Locate and identify every blood parasite.
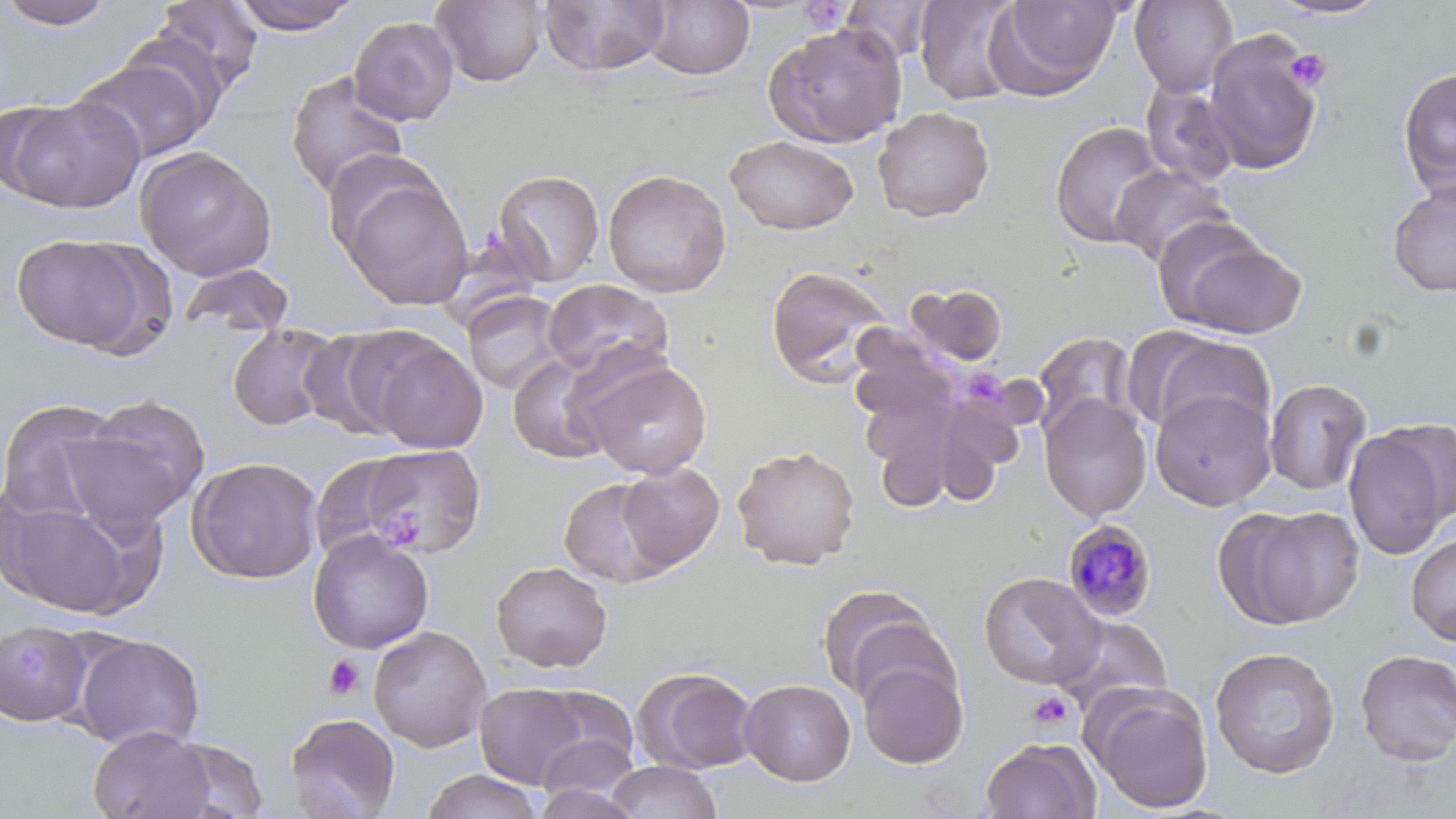

Approximate bounding boxes as (x1,y1)-(x2,y2) corner pairs in pixels.
Plasmodium malariae-infected red blood cells: (1062,519)-(1159,621).
No Plasmodium falciparum, Plasmodium ovale, Plasmodium vivax, Babesia divergens, or Trypanosoma brucei observed.

{
  "slide_level_diagnosis": "Plasmodium malariae",
  "image_size": "1456×819 pixels",
  "platelet_locations": "approximate bounding boxes as (x1,y1)-(x2,y2) corner pairs in pixels: (798,3)-(852,32), (1285,48)-(1332,93), (969,373)-(1004,406), (383,511)-(425,545), (16,644)-(54,678), (323,655)-(365,701), (1026,690)-(1075,732)",
  "stain": "May-Grünwald-Giemsa",
  "preparation": "thin blood smear",
  "modality": "light microscopy",
  "magnification": "1000x",
  "field_of_view": "one of a larger specimen",
  "uninfected_red_blood_cell_locations": "approximate bounding boxes as (x1,y1)-(x2,y2) corner pairs in pixels: (151,0)-(265,95), (228,0)-(363,35), (431,0)-(548,88), (537,0)-(671,78), (913,0)-(1024,105), (988,0)-(1123,99), (1129,0)-(1238,98), (2,1)-(116,29), (644,1)-(754,80), (839,1)-(939,62), (1264,1)-(1395,21), (348,16)-(459,125), (763,22)-(907,148), (1203,30)-(1325,176), (75,55)-(214,164), (1397,67)-(1456,197), (285,71)-(410,201), (1140,82)-(1241,187), (2,95)-(144,213), (872,107)-(995,222), (1049,121)-(1167,249), (725,135)-(859,235), (135,146)-(277,281), (1110,164)-(1233,267), (603,169)-(731,298), (492,170)-(605,287), (340,174)-(473,309), (1387,179)-(1456,296), (1163,230)-(1307,338), (11,232)-(163,357), (176,262)-(297,340), (765,264)-(894,388), (542,278)-(672,380), (906,283)-(1008,366), (462,291)-(567,395), (227,323)-(344,431), (298,326)-(414,441), (1134,330)-(1275,439), (1031,331)-(1140,443), (365,335)-(488,454), (507,352)-(615,465), (579,356)-(712,479), (1264,378)-(1371,495), (1150,389)-(1277,511), (70,394)-(211,529), (1039,395)-(1152,522), (0,399)-(124,523), (1343,424)-(1451,561), (359,443)-(485,558), (732,443)-(861,570), (309,453)-(422,562), (187,456)-(322,584), (617,462)-(725,572), (560,478)-(672,588), (2,494)-(149,618), (1222,504)-(1366,630), (307,530)-(434,654), (1406,533)-(1456,646), (490,561)-(613,673), (978,572)-(1104,690), (816,583)-(946,706), (1051,614)-(1174,717), (369,626)-(491,752), (0,627)-(107,726), (72,632)-(207,752), (1209,646)-(1341,779), (1354,649)-(1456,766), (855,654)-(969,769), (634,667)-(760,775), (739,679)-(856,786), (474,683)-(591,789), (529,684)-(639,776), (1085,684)-(1215,814), (284,712)-(401,818), (89,726)-(215,819), (534,733)-(640,809), (164,735)-(271,818), (980,736)-(1101,819), (605,760)-(723,818), (420,769)-(544,819), (530,784)-(646,819)"
}